Give the position of every Plasmodium parasite.
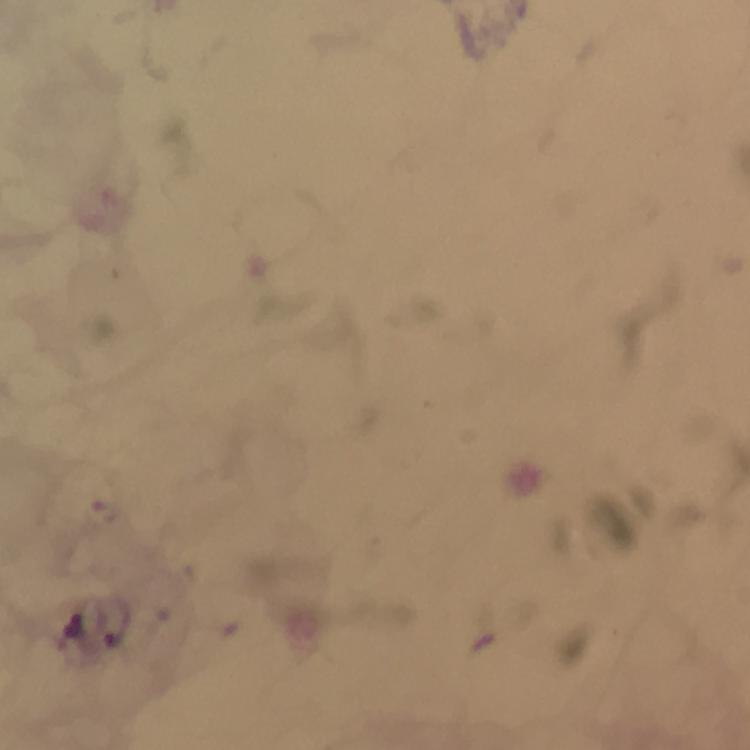

Approximate centers as (x, y) in pixels.
Plasmodium parasites: (73, 624).

Image is 750×750 pixels. Giemsa stain. Thick blood smear. 100x magnification. Immersion oil applied. A crop from one field of view. From a diagnostic examination for malaria. Photographed through the microscope with a smartphone camera.